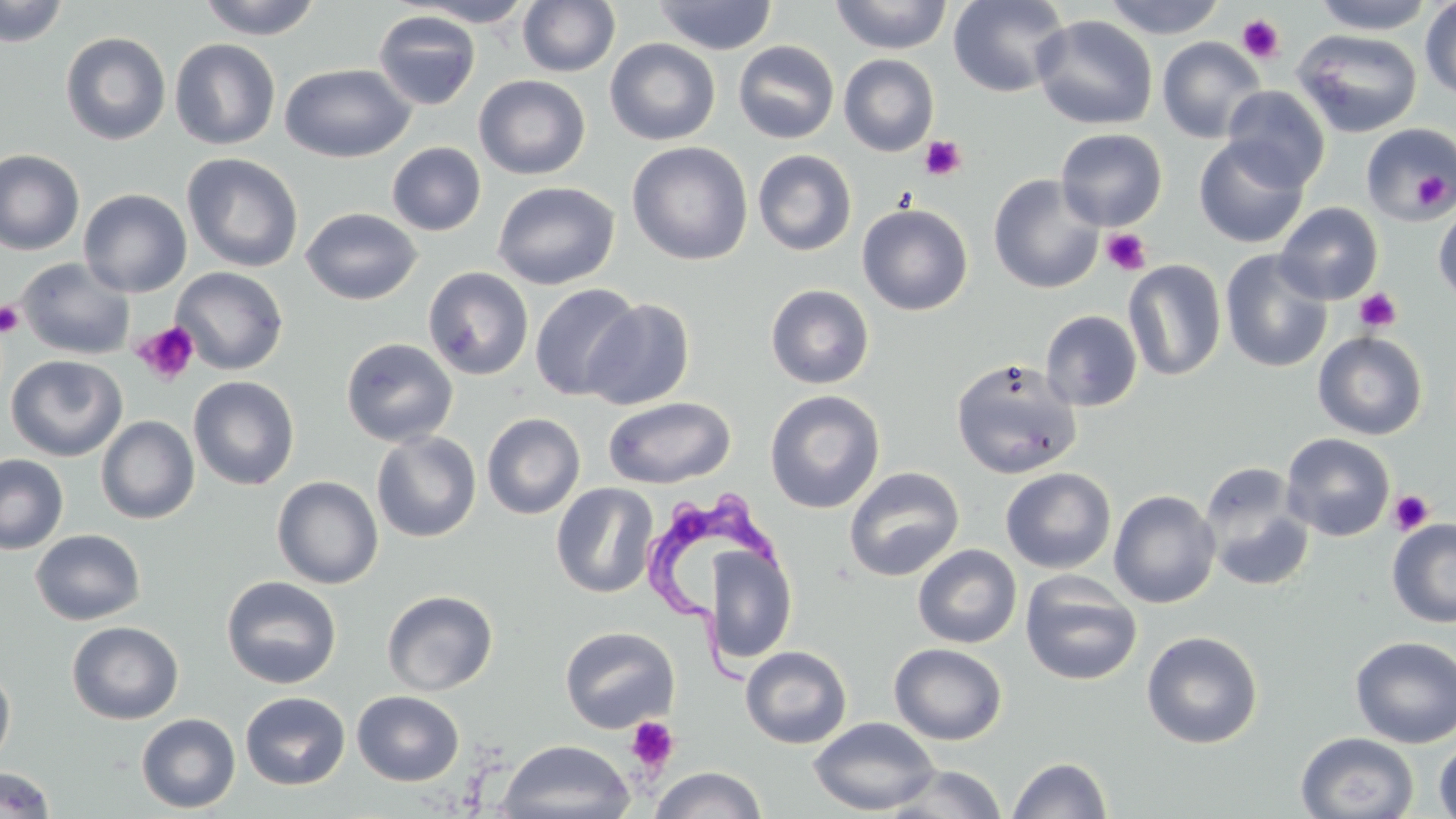
slide_level_diagnosis: Trypanosoma brucei
uninfected_red_blood_cell_locations: 'approximate bounding boxes as (x1, y1, x2, y2) in pixels: (0, 0, 69, 47), (197, 0, 323, 40), (652, 0, 779, 55), (830, 0, 953, 54), (948, 0, 1070, 97), (1102, 0, 1226, 39), (1311, 0, 1437, 34), (405, 1, 537, 27), (517, 1, 620, 77), (1420, 1, 1456, 102), (373, 10, 481, 110), (1032, 15, 1158, 130), (1293, 28, 1422, 138), (60, 31, 171, 145), (1157, 36, 1266, 143), (169, 38, 281, 151), (604, 38, 721, 146), (733, 40, 840, 144), (838, 53, 939, 156), (279, 63, 415, 163), (474, 74, 590, 180), (1222, 85, 1330, 192), (1360, 122, 1456, 224), (1056, 128, 1167, 231), (1193, 136, 1310, 249), (628, 141, 753, 265), (387, 142, 486, 235), (0, 149, 85, 256), (752, 149, 857, 256), (182, 153, 303, 272), (988, 174, 1104, 294), (492, 181, 620, 290), (78, 188, 192, 297), (856, 197, 1105, 305), (1433, 199, 1456, 308), (1276, 202, 1384, 304), (857, 203, 973, 316), (300, 207, 422, 305), (1220, 249, 1334, 373), (16, 257, 135, 360), (1123, 260, 1226, 381), (170, 266, 289, 375), (423, 266, 534, 380), (529, 283, 642, 402), (765, 284, 875, 390), (584, 297, 695, 410), (1040, 310, 1143, 411), (1313, 331, 1428, 440), (340, 336, 458, 447), (6, 354, 127, 461), (950, 358, 1082, 479), (188, 375, 300, 491), (764, 390, 885, 514), (603, 396, 736, 489), (482, 412, 585, 519), (96, 415, 200, 524), (370, 430, 481, 543), (1281, 433, 1395, 541), (0, 454, 69, 555), (843, 466, 965, 582), (1000, 467, 1117, 574), (1200, 467, 1315, 591), (272, 475, 384, 589), (551, 482, 660, 598), (1108, 489, 1221, 608), (1387, 518, 1456, 628), (30, 528, 146, 626), (708, 544, 796, 664), (912, 544, 1022, 648), (1020, 571, 1142, 686), (221, 576, 342, 689), (382, 589, 499, 696), (66, 621, 184, 724), (559, 625, 680, 734), (1141, 630, 1264, 749), (1349, 636, 1456, 749), (889, 642, 1008, 746), (740, 645, 852, 749), (0, 664, 16, 771), (240, 691, 350, 790), (351, 691, 464, 785), (136, 713, 241, 813), (808, 716, 940, 815), (1295, 732, 1419, 818), (496, 739, 634, 819), (1434, 739, 1456, 819), (1007, 757, 1113, 818), (881, 764, 1008, 818), (0, 766, 55, 817), (649, 767, 768, 819)'
magnification: 1000x
modality: light microscopy
stain: May-Grünwald-Giemsa
image_size: 1456×819 pixels
preparation: thin blood film
trypanosoma_brucei_locations: 'approximate bounding boxes as (x1, y1, x2, y2) in pixels: (643, 483, 783, 690)'
field_of_view: single
platelet_locations: 'approximate bounding boxes as (x1, y1, x2, y2) in pixels: (1237, 14, 1286, 64), (919, 135, 966, 181), (1412, 168, 1452, 212), (1101, 228, 1151, 275), (1354, 287, 1402, 333), (0, 300, 25, 336), (133, 321, 200, 386), (1388, 489, 1434, 535), (625, 717, 680, 774)'